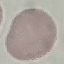
Summary:
  - Result: negative for malaria parasites
  - Stain: Giemsa
  - Image type: automatically extracted cell patch, resized to 64 × 64 pixels
  - Preparation: thin blood smear
  - Capture: smartphone through the microscope eyepiece